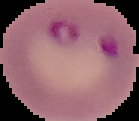
{
  "image_type": "segmented cell region on a black background",
  "image_size": "139×121 pixels",
  "preparation": "thin blood film",
  "malaria_status": "parasitized"
}